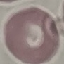
Summary:
  - Result: no malaria parasites detected
  - Stain: Giemsa
  - Image type: automatically extracted cell patch, resized to 64 × 64 pixels
  - Capture: smartphone through the microscope eyepiece
  - Preparation: thin blood smear